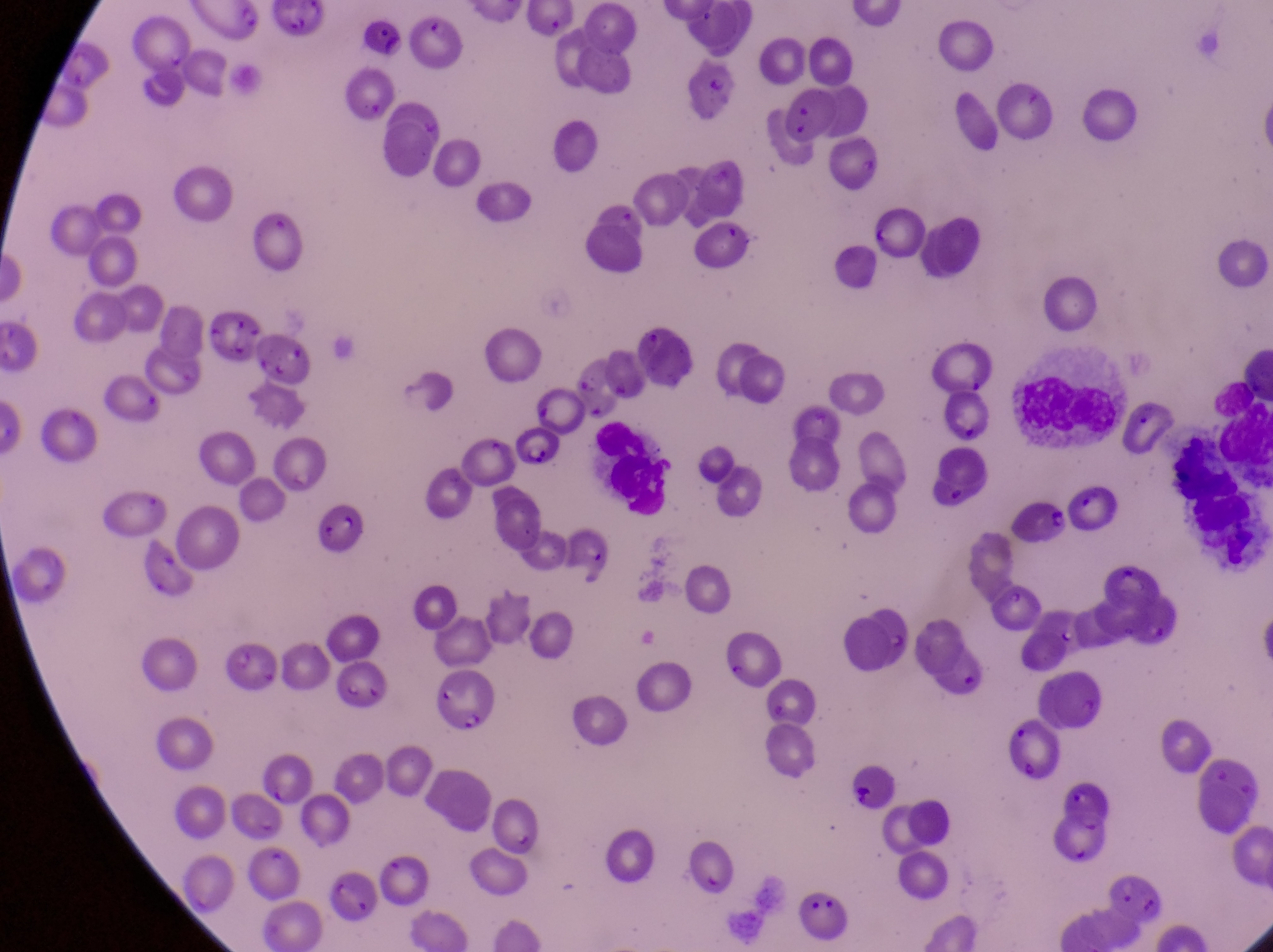

Approximate bounding boxes as (left, top, right, bottom) in pixels.
Summary:
  - Leukocyte locations: (1003, 360, 1118, 442), (1210, 376, 1271, 462), (586, 414, 671, 519)
  - Artifact (platelet-like body, stain precipitate, or debris) locations: (209, 307, 271, 369), (310, 499, 379, 573)
  - Parasitised red blood cell locations: (1125, 385, 1177, 460), (1009, 492, 1072, 550), (225, 635, 275, 692), (427, 669, 505, 739), (998, 705, 1058, 779)
  - Magnification: 1000x
  - Capture: smartphone photograph through the eyepiece of an Olympus CX-23 microscope
  - Preparation: thin blood smear
  - Image size: 1273×952 pixels
  - Country: Uganda
  - Field of view: single